Outline each Plasmodium vivax-infected red blood cell.
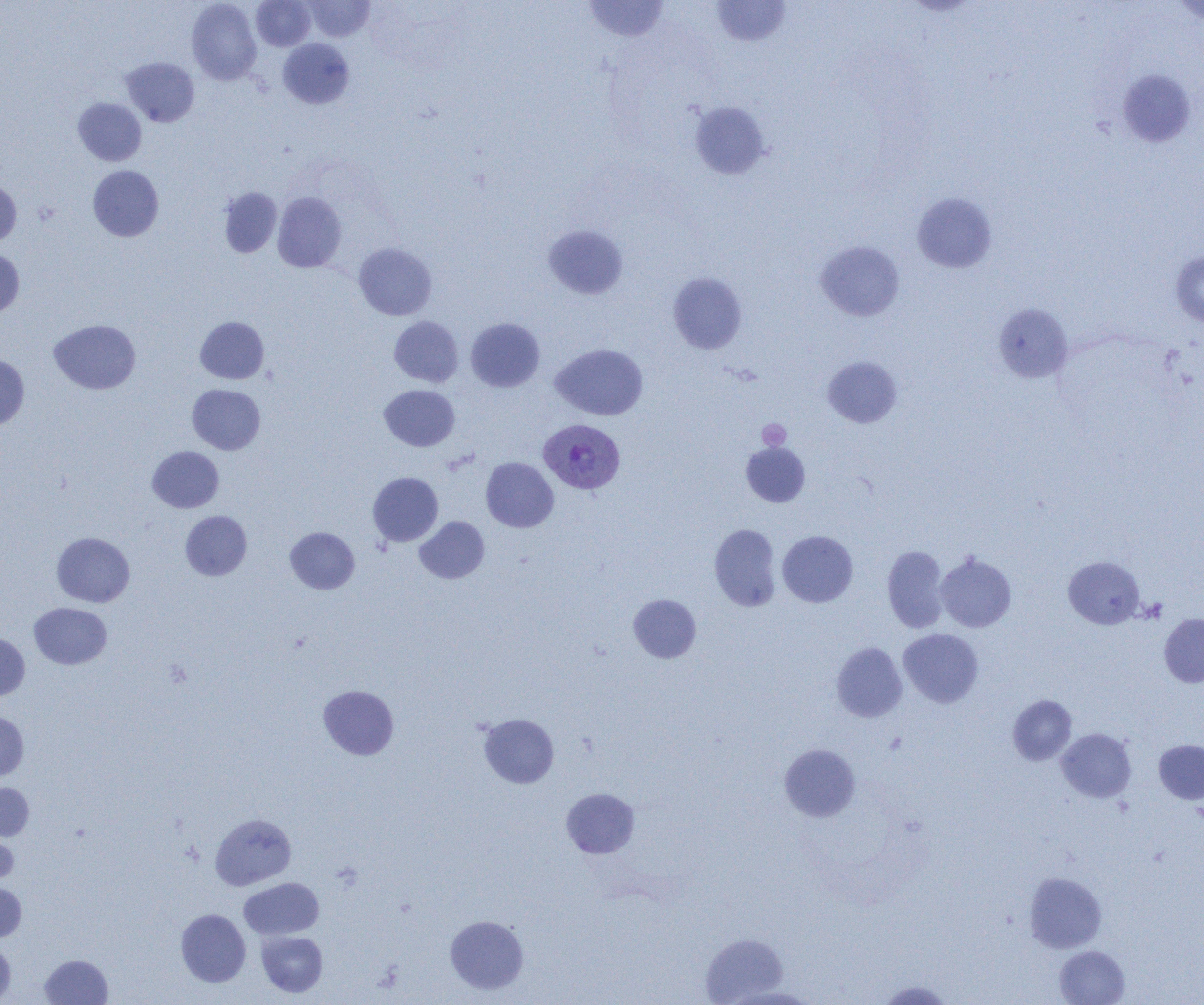
Approximate bounding boxes as (x1,y1)-(x2,y2) corner pairs in pixels.
Plasmodium vivax-infected red blood cells: (539,418)-(625,494).

Platelet locations: (757,419)-(791,450). Uninfected red blood cell locations: (187,0)-(261,84), (251,0)-(315,51), (303,0)-(375,42), (582,0)-(670,42), (711,0)-(791,47), (1170,1)-(1204,23), (278,38)-(355,108), (120,57)-(199,126), (1116,69)-(1197,147), (73,97)-(146,166), (690,101)-(771,180), (88,165)-(164,241), (0,177)-(21,246), (219,187)-(282,257), (272,192)-(346,272), (912,192)-(997,273), (543,225)-(628,299), (816,240)-(904,321), (353,242)-(437,320), (0,249)-(24,320), (1170,251)-(1204,326), (668,272)-(747,354), (993,303)-(1074,383), (195,316)-(269,384), (389,316)-(463,387), (466,318)-(545,392), (49,319)-(140,394), (551,343)-(648,420), (0,354)-(29,429), (822,356)-(902,427), (187,384)-(265,454), (379,385)-(459,451), (741,442)-(810,506), (147,446)-(224,512), (481,457)-(558,532), (368,472)-(443,546), (180,511)-(252,580), (415,516)-(489,583), (710,524)-(781,611), (286,527)-(359,594), (777,530)-(858,607), (52,532)-(135,607), (883,545)-(948,632), (935,553)-(1016,632), (1063,556)-(1145,629), (628,594)-(701,663), (29,602)-(112,669), (1159,613)-(1204,687), (898,628)-(983,708), (0,633)-(30,700), (831,642)-(907,722), (319,685)-(399,759), (1008,695)-(1077,765), (0,712)-(29,781), (479,713)-(558,788), (1057,728)-(1136,803), (1154,740)-(1204,804), (779,744)-(860,822), (0,783)-(33,840), (561,788)-(639,859), (210,814)-(296,890), (0,829)-(18,885), (1024,872)-(1107,953), (239,878)-(324,939), (0,883)-(26,941), (176,908)-(251,987), (445,915)-(529,994), (256,931)-(327,997), (700,933)-(787,1004), (0,939)-(15,1003), (1055,945)-(1130,1005), (40,954)-(112,1005), (876,981)-(954,1004). Slide-level diagnosis: Plasmodium vivax. One field of a larger specimen. Thin blood smear. Optical microscopy. Image is 1204×1005 pixels. Captured at 1000x magnification.